Point out each Plasmodium parasite.
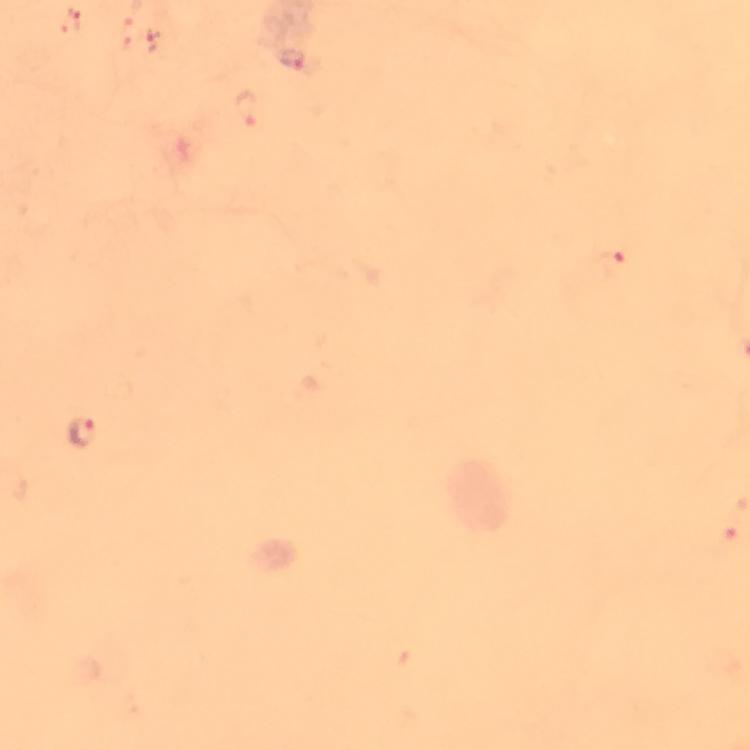

Approximate centers as [x, y] in pixels.
Plasmodium parasites: [292, 60], [246, 109], [615, 265], [82, 429].

Immersion oil was used. Photographed with a smartphone mounted on the microscope. Giemsa stain. Image is 750×750 pixels. At 100x magnification. A crop from one field of view. From a malaria diagnostic workup. Thick blood film.